Point out each leukocyte.
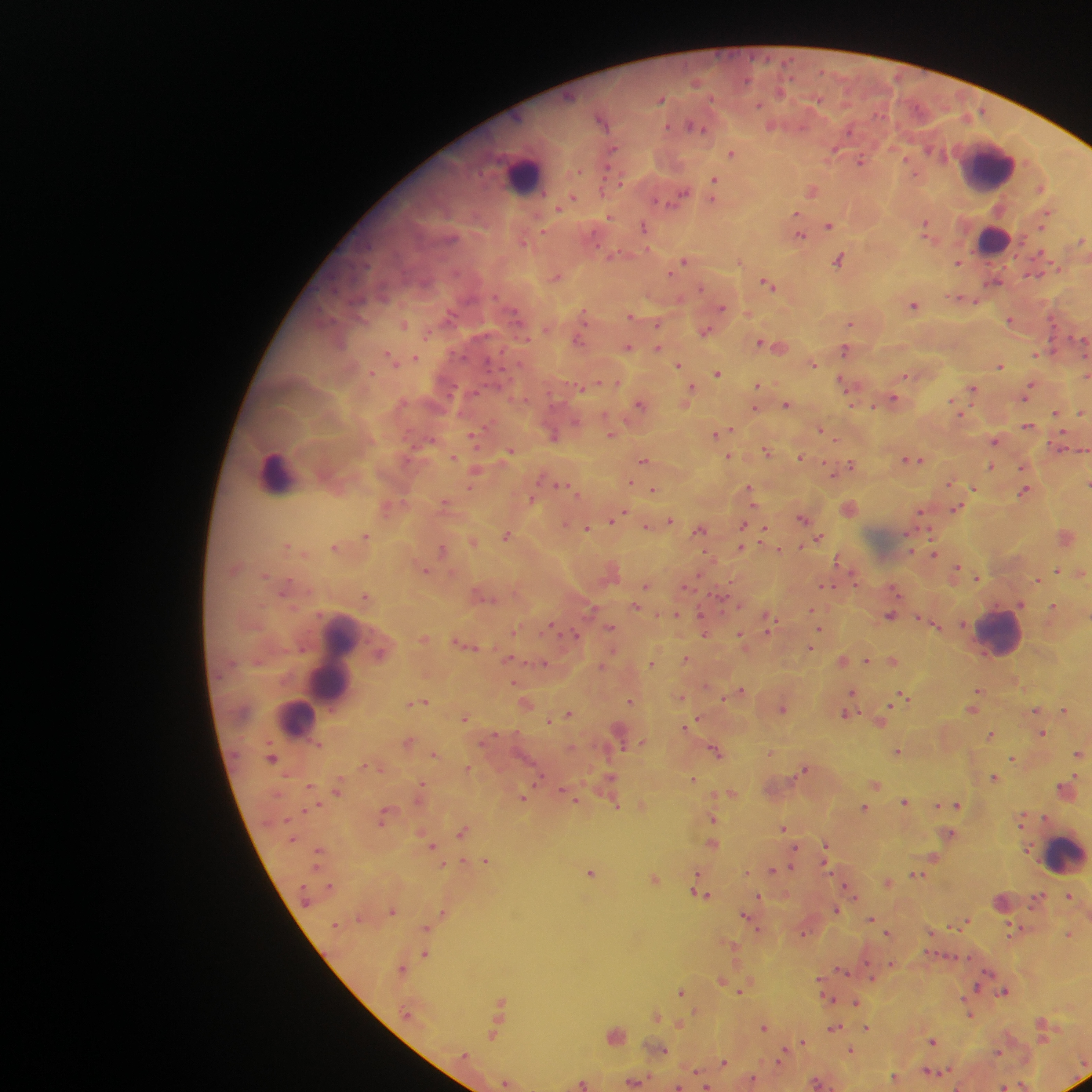

Approximate centers as x y in pixels.
Leukocytes: 991 167; 524 177; 992 239; 276 469; 1000 632; 332 661; 297 717; 1063 853.

Summary:
  - Malaria parasite locations: 746 80; 696 83; 780 91; 661 99; 817 100; 758 105; 602 121; 772 126; 695 127; 850 129; 613 150; 930 151; 833 152; 731 153; 860 161; 714 180; 1040 188; 812 191; 683 195; 573 198; 713 200; 661 202; 566 203; 559 208; 796 214; 609 217; 1044 218; 926 224; 829 225; 643 227; 543 230; 800 234; 1081 241; 523 242; 614 254; 839 260; 958 261; 683 262; 740 262; 670 273; 1033 274; 557 277; 994 280; 768 284; 701 288; 955 298; 965 298; 973 301; 913 305; 723 307; 449 316; 630 316; 324 317; 584 317; 1010 320; 850 322; 404 325; 657 325; 705 332; 1079 338; 578 341; 760 342; 628 347; 658 347; 780 347; 845 350; 1035 355; 390 357; 416 357; 813 363; 679 365; 999 366; 717 373; 1087 373; 906 375; 841 382; 758 385; 690 388; 973 389; 1028 390; 893 399; 953 403; 640 405; 787 405; 873 406; 755 409; 1056 412; 1081 412; 575 422; 1028 426; 821 430; 716 433; 553 435; 611 435; 472 436; 995 441; 509 451; 767 451; 729 456; 800 456; 454 457; 643 459; 914 460; 851 464; 991 467; 630 482; 949 483; 1087 483; 470 486; 563 486; 750 488; 973 488; 653 490; 1025 491; 531 499; 445 503; 957 509; 920 513; 619 515; 801 518; 613 520; 670 521; 565 525; 743 525; 648 526; 587 529; 765 529; 700 530; 366 536; 505 536; 1066 537; 818 538; 287 547; 333 547; 741 548; 442 549; 934 552; 840 562; 956 570; 1057 570; 425 571; 1082 573; 265 575; 978 577; 1037 580; 645 586; 828 586; 895 590; 366 596; 1021 604; 636 606; 1053 607; 591 609; 812 610; 676 615; 890 616; 769 623; 551 626; 935 626; 610 627; 704 629; 513 631; 819 631; 575 634; 741 635; 811 647; 380 653; 509 659; 686 659; 866 660; 844 661; 893 661; 653 662; 545 663; 602 666; 741 690; 852 691; 977 691; 681 697; 902 697; 630 701; 422 702; 527 704; 783 708; 972 709; 1036 711; 1065 711; 568 713; 846 714; 464 717; 549 721; 882 721; 688 726; 1043 734; 991 735; 408 742; 641 743; 715 750; 898 752; 1078 753; 434 754; 271 757; 1013 758; 469 768; 804 769; 994 777; 611 779; 693 779; 875 784; 422 785; 337 787; 1067 788; 564 792; 731 793; 524 796; 905 801; 617 805; 936 806; 958 806; 864 807; 383 818; 1022 818; 713 819; 784 827; 463 832; 949 834; 713 844; 431 845; 825 846; 934 858; 485 861; 793 861; 773 870; 590 872; 916 875; 655 879; 888 883; 330 886; 701 894; 1070 895; 759 898; 835 909; 393 911; 443 912; 744 915; 871 919; 967 921; 426 928; 1012 930; 803 932; 888 932; 1069 934; 426 954; 402 969; 841 970; 872 977; 722 980; 977 987; 742 989; 681 991; 1004 991; 855 1002; 501 1003; 656 1015; 970 1015; 679 1023; 764 1027; 867 1027; 834 1028; 494 1035; 802 1042; 932 1042; 661 1050; 851 1051; 781 1057; 724 1062; 929 1072; 944 1072; 895 1076; 752 1079; 507 1082; 634 1082; 582 1083; 817 1083; 677 1086; 1003 1086
  - Image size: 1092×1092 pixels
  - Preparation: thick blood film
  - Capture: mobile-phone photograph through a microscope
  - Country: Ghana
  - Field of view: single